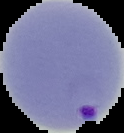

From a thin blood smear. Segmented cell region on a black background. Malaria status: parasitized. Image is 124×133 pixels.